State which parasite is depicted.
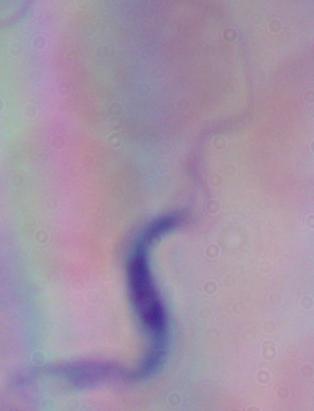
A trypanosome.

Summary:
  - Magnification: 1000x
  - Modality: micrograph